Locate every Plasmodium parasite.
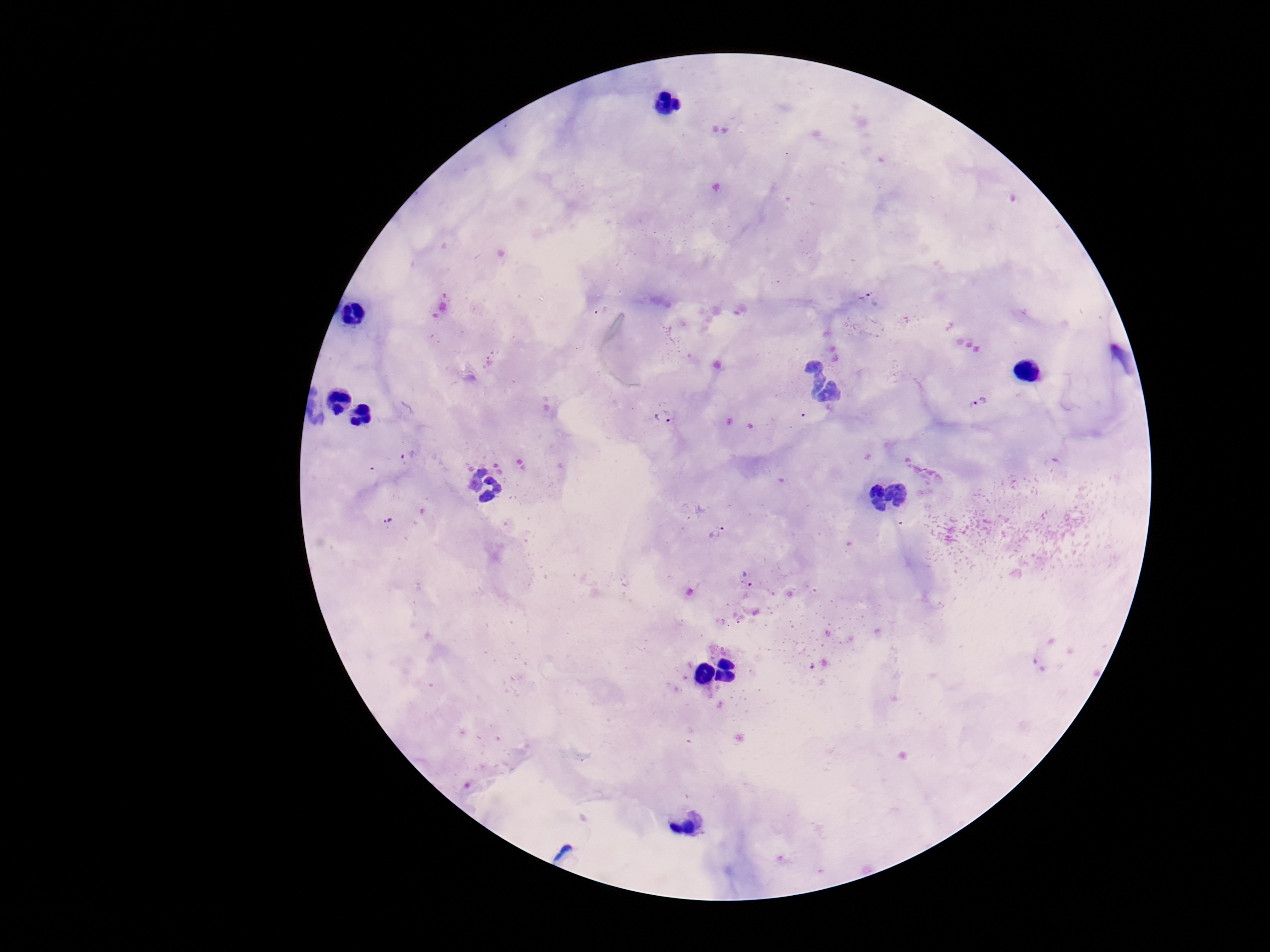

Approximate centers as [x, y] in pixels.
Plasmodium parasites: [867, 297], [981, 401], [663, 416], [407, 457], [386, 522], [716, 532], [745, 580], [816, 665].

Summary:
  - Capture: smartphone camera through the microscope eyepiece
  - Image size: 1270×952 pixels
  - Magnification: 100x
  - Patient malaria status: infected
  - Field of view: one from this slide
  - Stain: Giemsa
  - Preparation: thick peripheral-blood smear